Assess this cell for malaria.
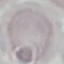

It is uninfected.

{
  "image_type": "cell patch, automatically extracted from a larger field of view and resized to 64 × 64 pixels",
  "stain": "Giemsa",
  "capture": "smartphone through the microscope eyepiece",
  "preparation": "thin smear"
}